Assess the morphology of the red blood cells.
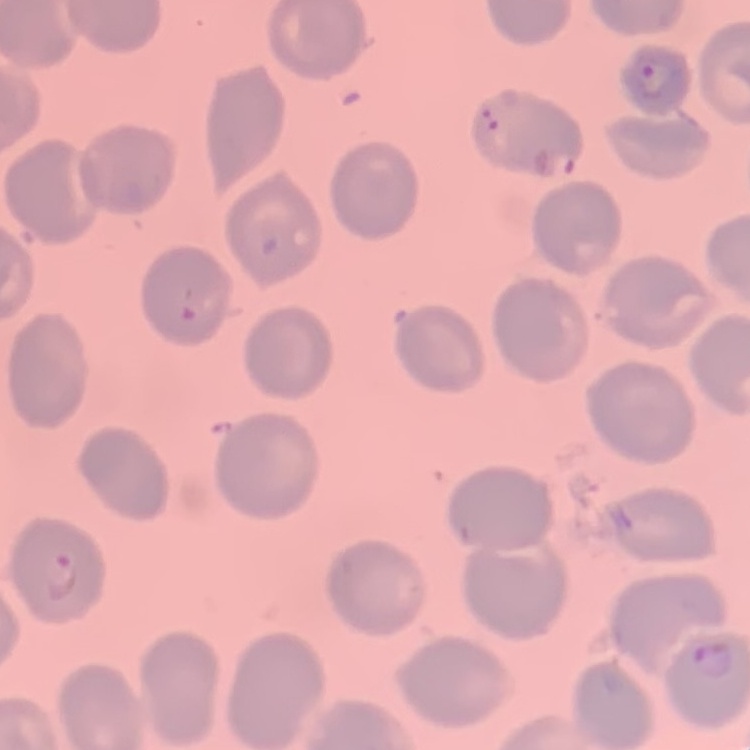

They show no rouleaux formation.

Summary:
  - Preparation: thin blood film
  - Image type: square crop of a larger photomicrograph
  - Stain: Field's or Giemsa